Locate every blood parasite and identify its species.
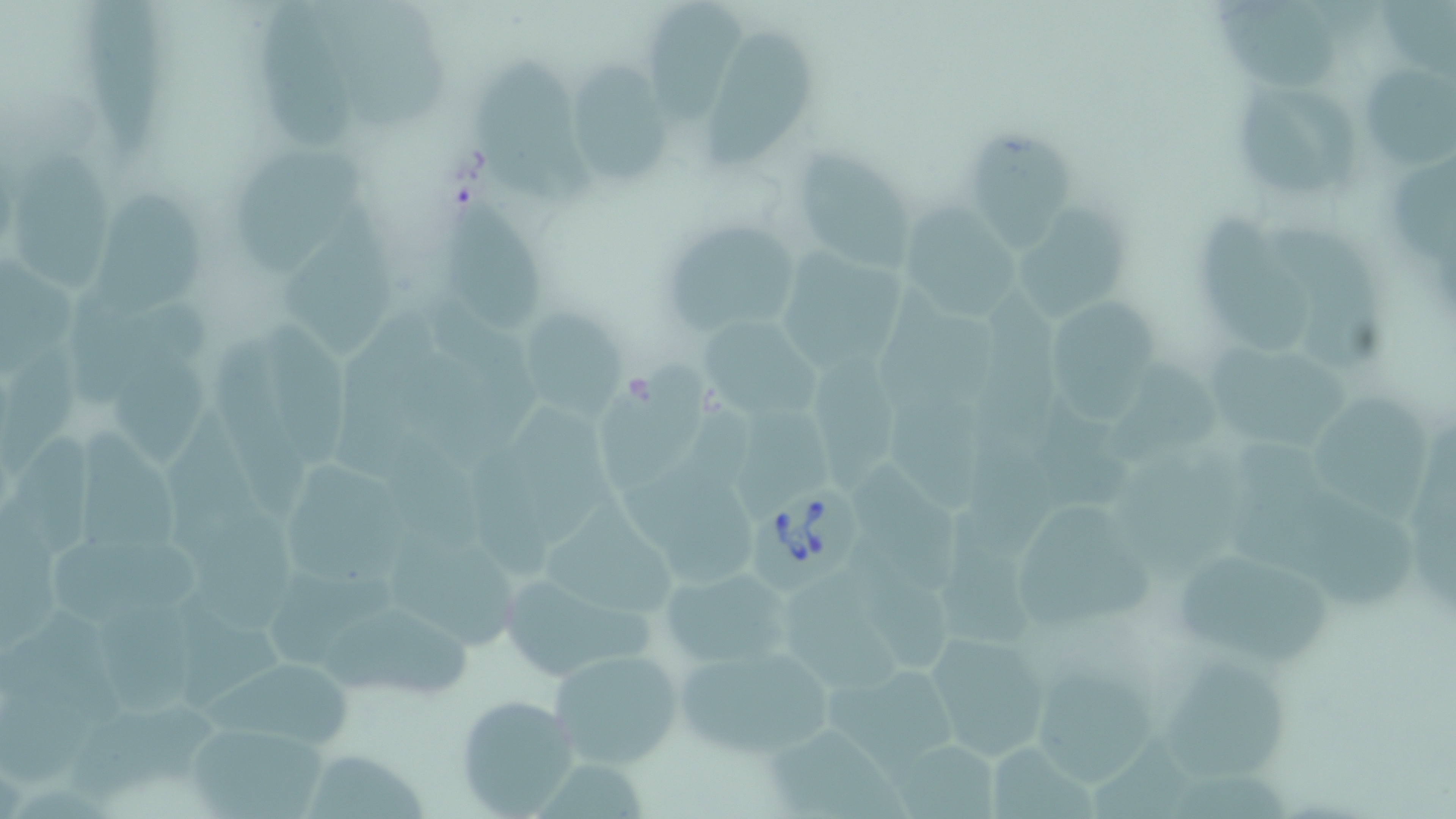

Approximate bounding boxes as named x1/y1/x2/y2 corners in pixels.
Babesia divergens-infected red blood cells: (x1=747, y1=483, x2=865, y2=604).
No Plasmodium falciparum, Plasmodium ovale, Plasmodium malariae, Plasmodium vivax, or Trypanosoma brucei observed.

Uninfected red blood cell locations: (x1=79, y1=1, x2=169, y2=165), (x1=252, y1=2, x2=358, y2=151), (x1=1385, y1=2, x2=1456, y2=80), (x1=328, y1=3, x2=459, y2=136), (x1=1213, y1=4, x2=1342, y2=90), (x1=645, y1=7, x2=742, y2=129), (x1=699, y1=32, x2=823, y2=174), (x1=474, y1=57, x2=603, y2=210), (x1=564, y1=59, x2=674, y2=193), (x1=1358, y1=63, x2=1455, y2=175), (x1=1234, y1=72, x2=1361, y2=198), (x1=968, y1=123, x2=1073, y2=257), (x1=794, y1=144, x2=918, y2=273), (x1=234, y1=148, x2=362, y2=282), (x1=11, y1=149, x2=108, y2=298), (x1=1393, y1=155, x2=1456, y2=268), (x1=438, y1=178, x2=555, y2=339), (x1=90, y1=194, x2=207, y2=321), (x1=903, y1=203, x2=1022, y2=320), (x1=1016, y1=203, x2=1125, y2=324), (x1=1193, y1=207, x2=1317, y2=352), (x1=283, y1=210, x2=398, y2=356), (x1=660, y1=218, x2=808, y2=338), (x1=1283, y1=221, x2=1384, y2=369), (x1=782, y1=249, x2=901, y2=373), (x1=0, y1=254, x2=81, y2=374), (x1=986, y1=301, x2=1073, y2=444), (x1=1051, y1=301, x2=1160, y2=425), (x1=70, y1=306, x2=211, y2=402), (x1=517, y1=307, x2=625, y2=421), (x1=698, y1=318, x2=825, y2=415), (x1=264, y1=325, x2=349, y2=471), (x1=212, y1=336, x2=316, y2=522), (x1=1203, y1=338, x2=1355, y2=453), (x1=0, y1=351, x2=89, y2=490), (x1=598, y1=355, x2=709, y2=497), (x1=105, y1=356, x2=207, y2=472), (x1=813, y1=357, x2=898, y2=491), (x1=1100, y1=364, x2=1224, y2=473), (x1=1314, y1=393, x2=1437, y2=515), (x1=738, y1=403, x2=830, y2=517), (x1=510, y1=404, x2=615, y2=539), (x1=10, y1=425, x2=101, y2=558), (x1=81, y1=426, x2=185, y2=554), (x1=391, y1=433, x2=481, y2=538), (x1=1234, y1=442, x2=1415, y2=612), (x1=1116, y1=445, x2=1250, y2=587), (x1=472, y1=457, x2=554, y2=583), (x1=625, y1=459, x2=760, y2=584), (x1=290, y1=460, x2=406, y2=582), (x1=850, y1=462, x2=968, y2=599), (x1=534, y1=493, x2=675, y2=612), (x1=1007, y1=503, x2=1157, y2=636), (x1=199, y1=506, x2=296, y2=640), (x1=935, y1=508, x2=1043, y2=647), (x1=390, y1=525, x2=516, y2=649), (x1=45, y1=535, x2=211, y2=624), (x1=860, y1=544, x2=969, y2=673), (x1=1175, y1=546, x2=1332, y2=664), (x1=502, y1=565, x2=655, y2=672), (x1=660, y1=567, x2=788, y2=669), (x1=267, y1=574, x2=414, y2=669), (x1=786, y1=574, x2=901, y2=693), (x1=178, y1=594, x2=285, y2=712), (x1=96, y1=606, x2=208, y2=716), (x1=321, y1=609, x2=476, y2=697), (x1=1, y1=612, x2=124, y2=790), (x1=925, y1=630, x2=1055, y2=762), (x1=671, y1=644, x2=836, y2=763), (x1=547, y1=648, x2=682, y2=769), (x1=1151, y1=656, x2=1287, y2=782), (x1=199, y1=660, x2=354, y2=753), (x1=1034, y1=663, x2=1160, y2=789), (x1=825, y1=667, x2=956, y2=780), (x1=454, y1=692, x2=583, y2=815), (x1=77, y1=709, x2=222, y2=804), (x1=765, y1=721, x2=909, y2=817), (x1=184, y1=726, x2=324, y2=816), (x1=1091, y1=734, x2=1193, y2=815), (x1=895, y1=735, x2=999, y2=816), (x1=991, y1=741, x2=1101, y2=817), (x1=307, y1=747, x2=430, y2=817). Slide-level diagnosis: Babesia divergens. Image is 1456×819 pixels. One field of a larger specimen. Thin blood smear. Optical microscopy. Captured at 1000x magnification. May-Grünwald-Giemsa-stained preparation.